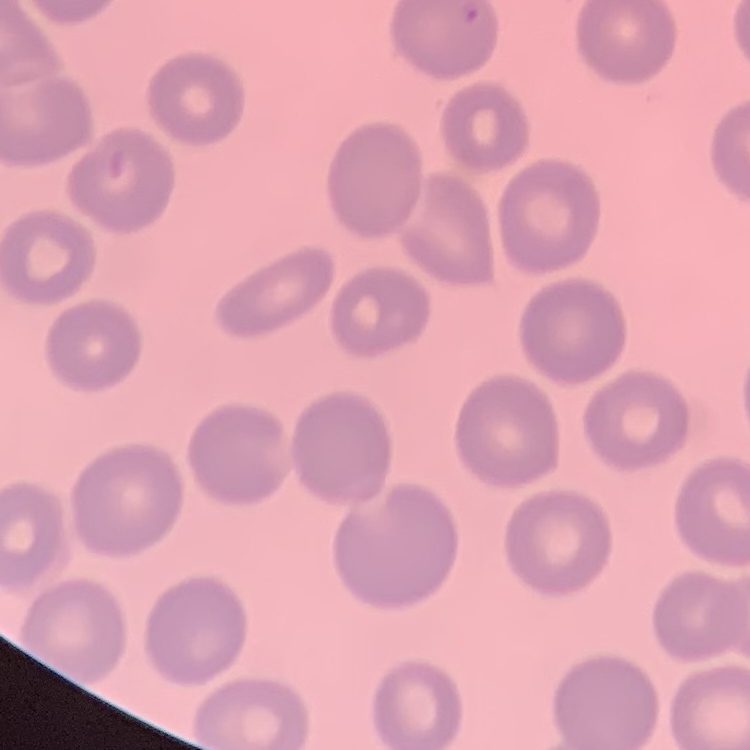

erythrocyte morphology = no rouleaux formation
stain = Field's or Giemsa
preparation = thin blood smear
image type = one tile cut from a larger photomicrograph